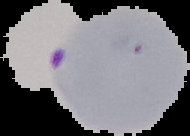

preparation: thin blood film
image_type: segmented cell region on a black background
result: Plasmodium parasites detected
image_size: 190×136 pixels